Report the malaria status of this cell.
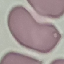

It is uninfected.

{
  "stain": "Giemsa",
  "preparation": "thin smear",
  "image_type": "automatically extracted cell patch, resized to 64 × 64 pixels",
  "capture": "smartphone camera at the microscope eyepiece"
}